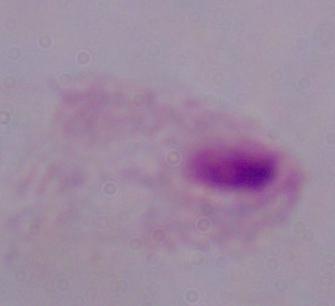
Captured at 1000x magnification. Micrograph. A trichomonad is seen.